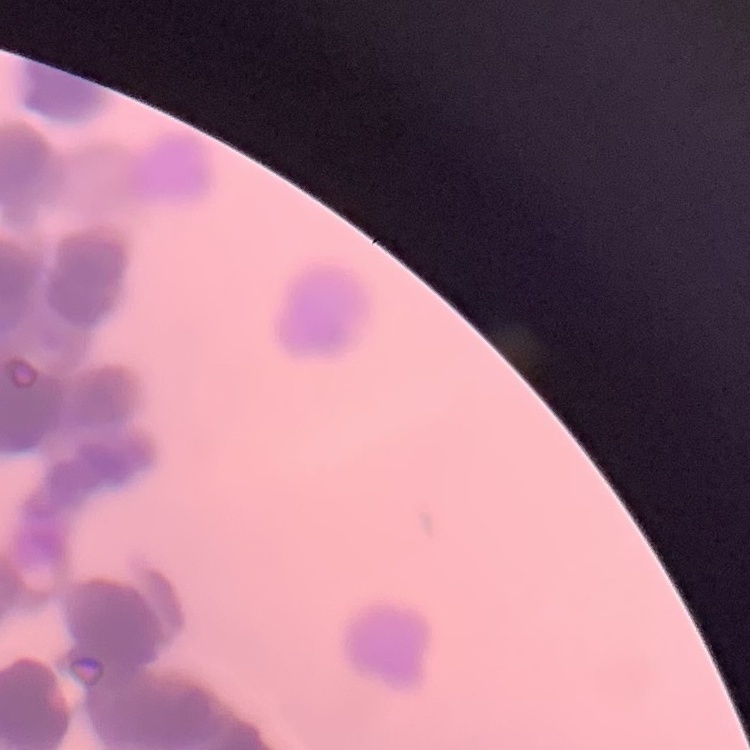

Summary:
  - Erythrocyte morphology: rouleaux formation
  - Preparation: thin peripheral smear
  - Stain: Field's or Giemsa
  - Image type: square crop of a larger photomicrograph